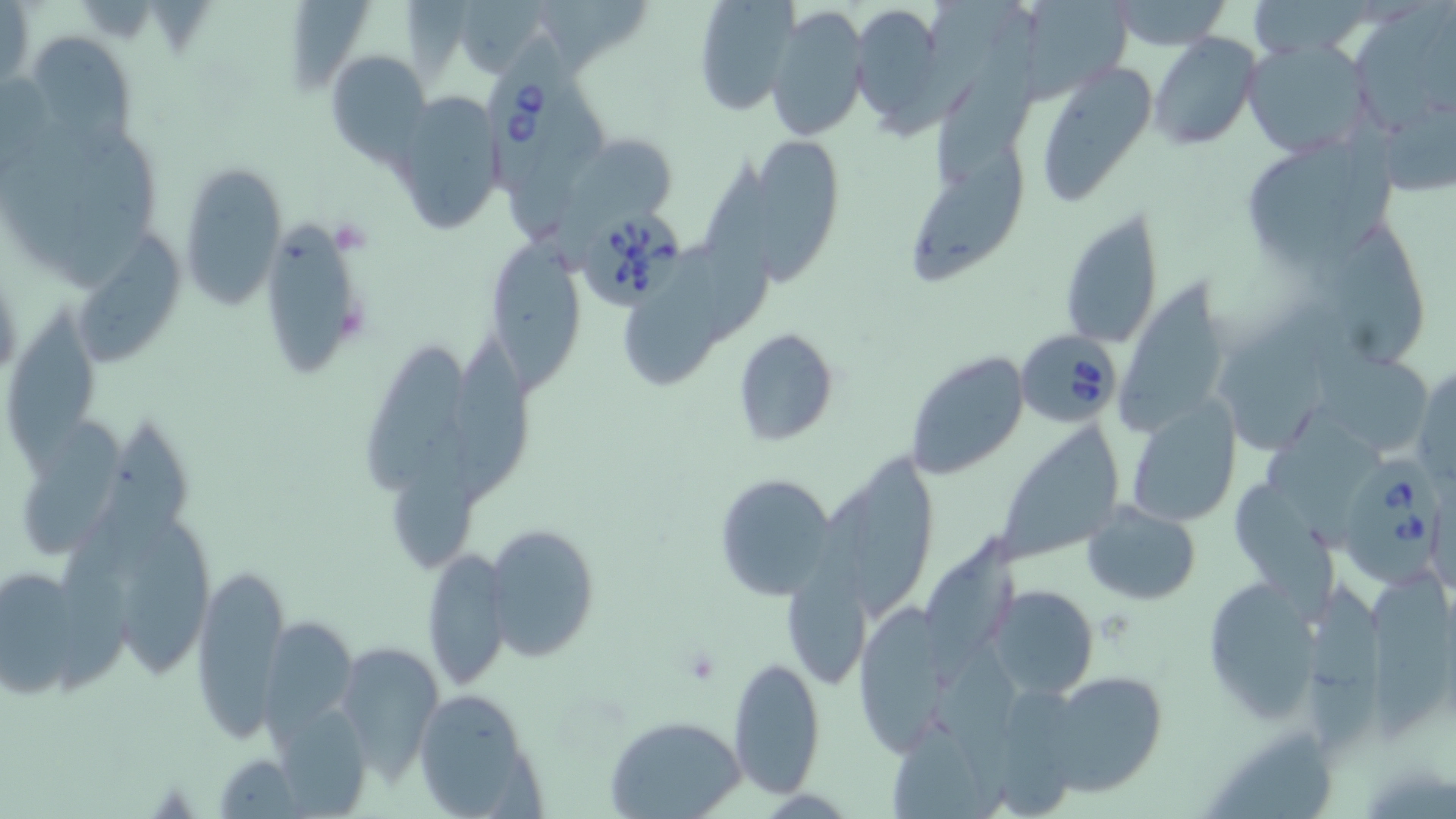
{
  "slide_level_diagnosis": "Babesia divergens",
  "preparation": "thin blood smear",
  "babesia_divergens_infected_red_blood_cell_locations": "approximate bounding boxes as named x1/y1/x2/y2 corners in pixels: (x1=479, y1=27, x2=575, y2=199), (x1=583, y1=211, x2=687, y2=308), (x1=1015, y1=331, x2=1122, y2=429), (x1=1333, y1=458, x2=1444, y2=589)",
  "modality": "optical microscopy",
  "magnification": "1000x",
  "image_size": "1456×819 pixels",
  "field_of_view": "single",
  "uninfected_red_blood_cell_locations": "approximate bounding boxes as named x1/y1/x2/y2 corners in pixels: (x1=690, y1=0, x2=799, y2=118), (x1=1111, y1=0, x2=1231, y2=50), (x1=848, y1=1, x2=949, y2=134), (x1=1, y1=3, x2=34, y2=91), (x1=1008, y1=3, x2=1137, y2=105), (x1=764, y1=4, x2=869, y2=143), (x1=1349, y1=7, x2=1456, y2=135), (x1=932, y1=13, x2=1040, y2=187), (x1=1149, y1=32, x2=1260, y2=151), (x1=25, y1=33, x2=135, y2=150), (x1=1241, y1=39, x2=1373, y2=160), (x1=326, y1=48, x2=432, y2=164), (x1=1034, y1=61, x2=1159, y2=206), (x1=387, y1=94, x2=505, y2=236), (x1=566, y1=131, x2=679, y2=225), (x1=1239, y1=135, x2=1395, y2=264), (x1=740, y1=137, x2=847, y2=272), (x1=907, y1=149, x2=1031, y2=287), (x1=694, y1=160, x2=776, y2=347), (x1=178, y1=162, x2=288, y2=310), (x1=1059, y1=207, x2=1165, y2=350), (x1=258, y1=212, x2=370, y2=380), (x1=1329, y1=222, x2=1427, y2=367), (x1=491, y1=234, x2=585, y2=403), (x1=76, y1=239, x2=186, y2=367), (x1=631, y1=241, x2=726, y2=389), (x1=1117, y1=280, x2=1230, y2=431), (x1=1219, y1=304, x2=1341, y2=464), (x1=6, y1=306, x2=98, y2=474), (x1=733, y1=326, x2=839, y2=447), (x1=442, y1=336, x2=532, y2=506), (x1=366, y1=347, x2=464, y2=494), (x1=904, y1=350, x2=1031, y2=481), (x1=1315, y1=353, x2=1437, y2=459), (x1=1413, y1=365, x2=1456, y2=485), (x1=1125, y1=400, x2=1243, y2=527), (x1=1261, y1=414, x2=1392, y2=549), (x1=18, y1=416, x2=124, y2=558), (x1=111, y1=418, x2=196, y2=576), (x1=387, y1=424, x2=496, y2=572), (x1=994, y1=424, x2=1127, y2=564), (x1=854, y1=446, x2=941, y2=622), (x1=713, y1=471, x2=838, y2=599), (x1=1233, y1=486, x2=1336, y2=622), (x1=792, y1=489, x2=888, y2=694), (x1=47, y1=501, x2=161, y2=706), (x1=1083, y1=501, x2=1200, y2=604), (x1=117, y1=514, x2=214, y2=683), (x1=484, y1=523, x2=599, y2=665), (x1=923, y1=535, x2=1031, y2=695), (x1=423, y1=546, x2=511, y2=691), (x1=0, y1=562, x2=100, y2=698), (x1=191, y1=564, x2=288, y2=745), (x1=1372, y1=568, x2=1452, y2=754), (x1=1199, y1=576, x2=1324, y2=725), (x1=1302, y1=583, x2=1390, y2=754), (x1=988, y1=585, x2=1097, y2=699), (x1=852, y1=605, x2=949, y2=750), (x1=263, y1=616, x2=356, y2=737), (x1=335, y1=640, x2=441, y2=779), (x1=934, y1=651, x2=1031, y2=813), (x1=727, y1=653, x2=826, y2=797), (x1=1036, y1=669, x2=1171, y2=798), (x1=412, y1=686, x2=544, y2=816), (x1=607, y1=716, x2=745, y2=819), (x1=887, y1=721, x2=997, y2=819), (x1=1209, y1=734, x2=1347, y2=818), (x1=211, y1=754, x2=302, y2=817)",
  "stain": "May-Grünwald-Giemsa"
}